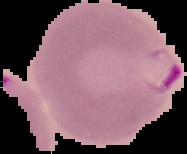
From a thin blood film. Segmented cell region on a black background. Malaria status: parasitized. Image is 187×154 pixels.